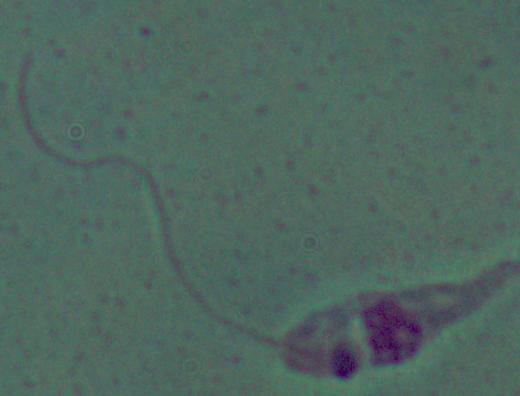

Summary:
  - Identification: Leishmania
  - Modality: photomicrograph
  - Magnification: 1000x